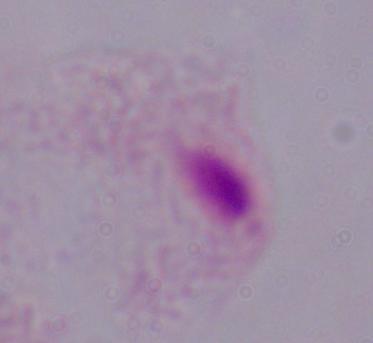

magnification = 1000x
modality = micrograph
identification = trichomonad